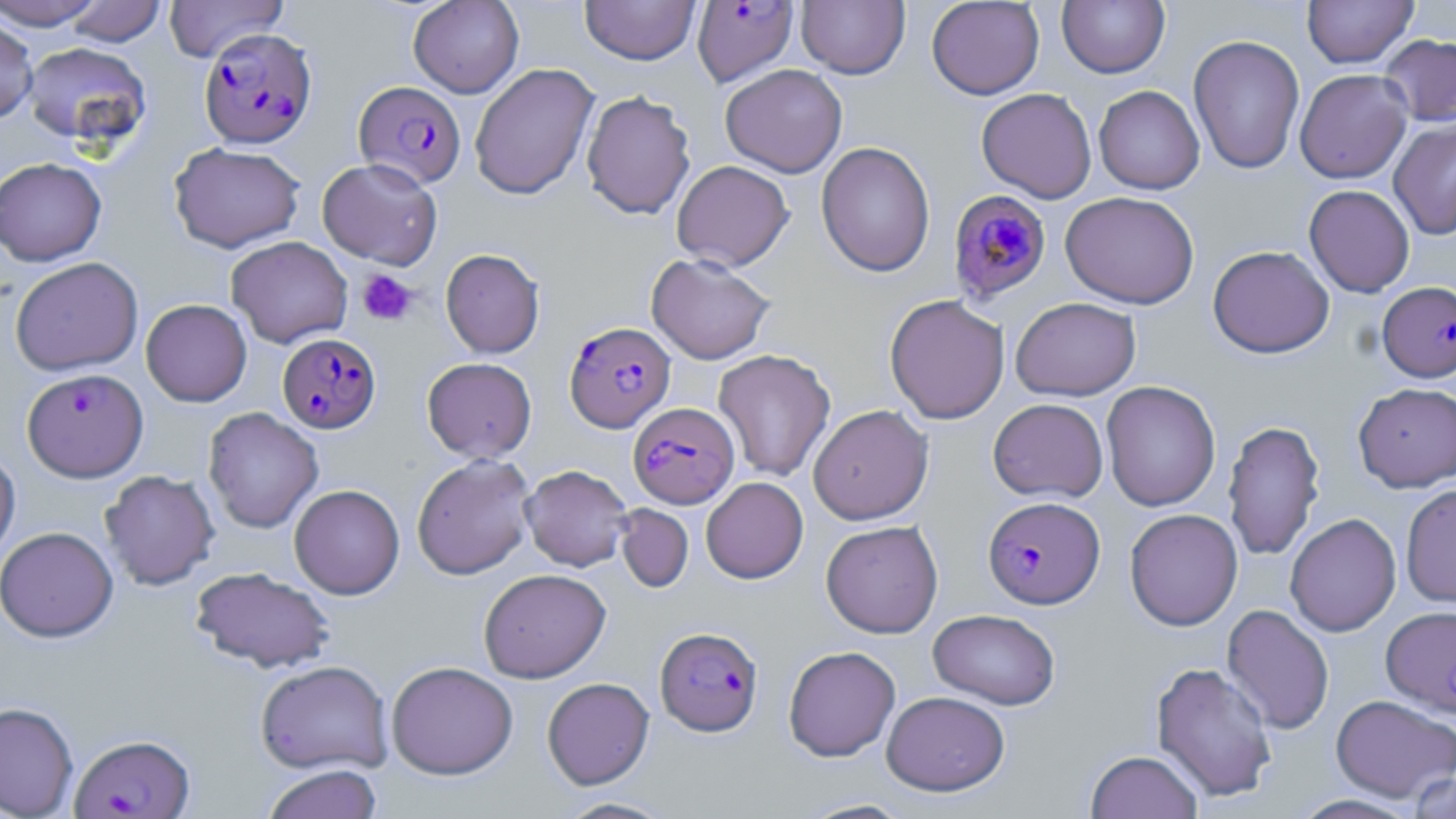 Approximate bounding boxes as (x1, y1, x2, y2) in pixels. Uninfected red blood cell locations: (0, 0, 108, 30), (162, 0, 289, 63), (408, 0, 524, 98), (580, 0, 701, 65), (926, 0, 1045, 99), (1057, 0, 1169, 78), (1302, 0, 1418, 67), (63, 1, 166, 46), (796, 1, 910, 79), (0, 16, 38, 126), (1188, 33, 1305, 175), (1379, 33, 1456, 127), (22, 42, 151, 148), (469, 63, 599, 200), (720, 63, 847, 178), (1294, 68, 1412, 183), (1093, 85, 1205, 195), (976, 88, 1097, 203), (581, 89, 696, 220), (1388, 118, 1456, 240), (816, 141, 935, 277), (169, 142, 305, 252), (0, 157, 107, 266), (317, 158, 443, 269), (671, 160, 794, 270), (1304, 185, 1415, 297), (1060, 191, 1199, 309), (226, 236, 353, 348), (1207, 245, 1334, 358), (440, 248, 545, 358), (646, 252, 776, 364), (10, 257, 143, 375), (884, 294, 1010, 424), (1010, 297, 1141, 401), (141, 299, 252, 406), (713, 349, 836, 482), (422, 357, 537, 462), (1101, 381, 1221, 512), (1353, 382, 1456, 492), (988, 398, 1109, 502), (808, 404, 933, 525), (203, 407, 324, 533), (1223, 419, 1325, 561), (0, 446, 20, 567), (412, 454, 536, 579), (520, 464, 633, 571), (100, 469, 220, 590), (700, 477, 808, 583), (1400, 483, 1456, 609), (289, 484, 405, 599), (615, 504, 693, 593), (1125, 509, 1243, 631), (1285, 513, 1401, 636), (821, 520, 943, 638), (0, 526, 119, 642), (190, 566, 336, 673), (478, 568, 610, 683), (1383, 603, 1456, 713), (1222, 604, 1334, 734), (928, 609, 1061, 709), (783, 645, 900, 762), (255, 659, 393, 775), (386, 661, 518, 780), (1151, 661, 1278, 804), (542, 677, 654, 789), (881, 691, 1009, 795), (1330, 694, 1456, 802), (0, 701, 79, 819), (1085, 750, 1203, 819), (261, 764, 383, 819), (1405, 769, 1456, 818), (554, 797, 678, 818), (795, 798, 916, 818). Plasmodium falciparum-infected red blood cell locations: (692, 1, 798, 87), (198, 26, 317, 149), (354, 80, 466, 188), (945, 184, 1050, 301), (1377, 281, 1456, 382), (564, 321, 675, 432), (277, 332, 381, 433), (22, 367, 148, 482), (628, 403, 738, 508), (982, 496, 1104, 609), (655, 627, 763, 736), (69, 733, 195, 818). Platelet locations: (357, 269, 418, 327). Slide-level diagnosis: Plasmodium falciparum. Thin blood smear. Light microscopy. Image is 1456×819 pixels. One field of a larger specimen. Captured at 1000x magnification. May-Grünwald-Giemsa stain.